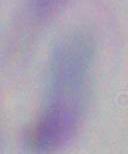 1000x magnification. Micrograph. Toxoplasma gondii is seen.